Describe the morphology of the red blood cells.
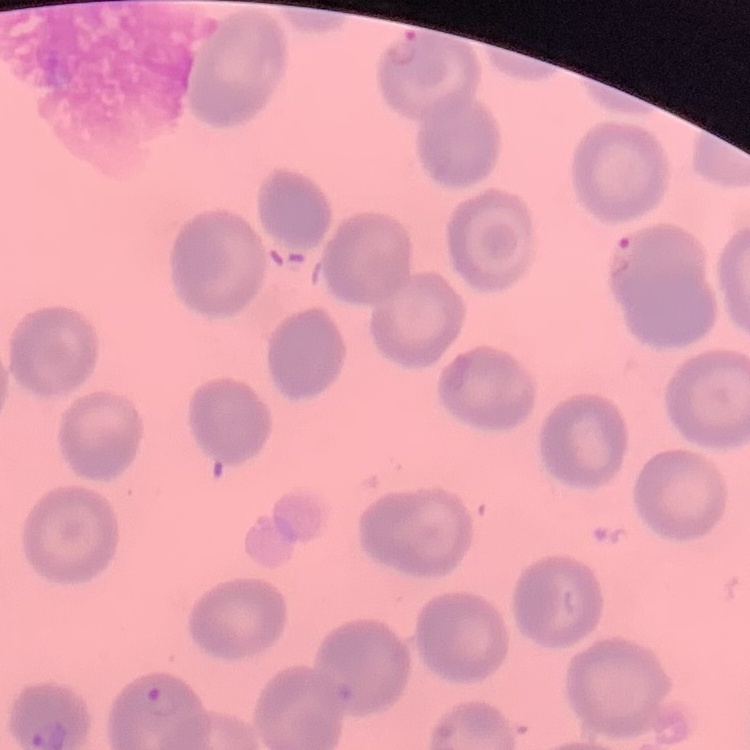

No rouleaux formation.

Summary:
  - Image type: one tile cut from a larger photomicrograph
  - Preparation: thin blood smear
  - Stain: Field's or Giemsa